Report the malaria status of this cell.
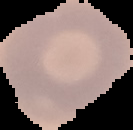
Uninfected.

The area outside the segmented cell region is set to black. From a thin blood smear. Image is 133×130 pixels.